Report the malaria status of this cell.
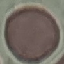

Uninfected.

Photographed with a smartphone camera at the microscope eyepiece. Thin blood film. Giemsa stain. Cell patch, automatically extracted from a larger field of view and resized to 64 × 64 pixels.